Classify this cell by malaria status.
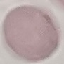
It is uninfected.

preparation: thin blood smear
image_type: automatically extracted cell patch, resized to 64 × 64 pixels
capture: smartphone camera at the microscope eyepiece
stain: Giemsa